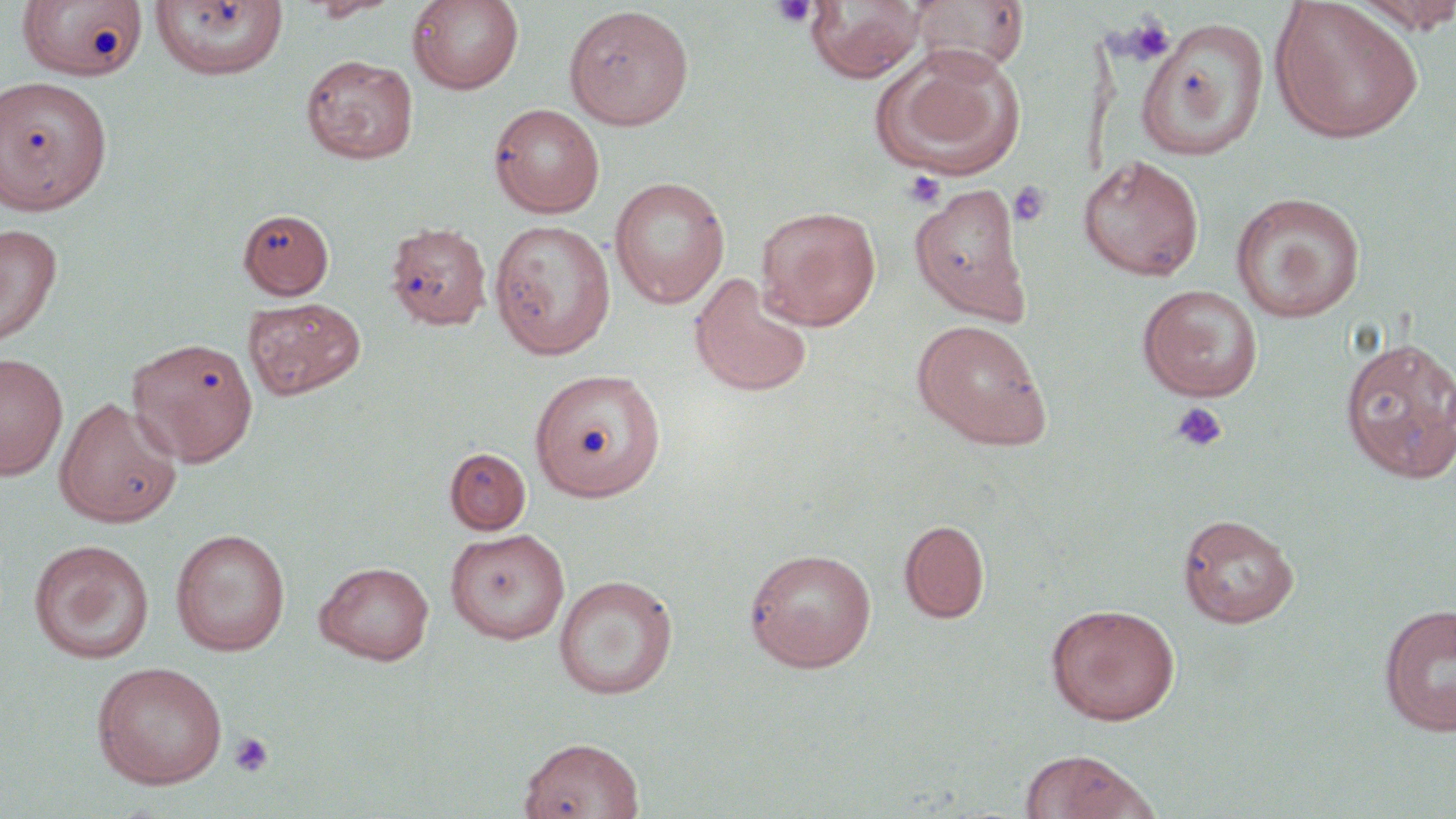

Summary:
  - Coordinate format: approximate bounding boxes as [x1, y1, x2, y2] in pixels
  - Platelet locations: [772, 0, 819, 27], [1119, 12, 1176, 65], [903, 171, 946, 208], [1008, 181, 1051, 227], [1171, 402, 1228, 453], [228, 732, 274, 777]
  - Uninfected red blood cell locations: [18, 0, 147, 82], [302, 0, 401, 22], [407, 0, 524, 94], [907, 0, 1030, 76], [149, 1, 289, 81], [806, 1, 924, 82], [1269, 1, 1424, 145], [1350, 1, 1456, 33], [563, 5, 694, 129], [1136, 17, 1270, 160], [872, 48, 1024, 180], [300, 53, 419, 164], [0, 76, 112, 216], [488, 103, 604, 218], [1078, 153, 1205, 282], [609, 176, 729, 309], [909, 183, 1031, 324], [1230, 192, 1366, 323], [755, 205, 881, 330], [238, 208, 335, 300], [489, 219, 616, 359], [384, 220, 493, 331], [0, 223, 62, 346], [689, 272, 814, 398], [1136, 283, 1264, 401], [243, 297, 366, 400], [911, 318, 1052, 450], [1338, 335, 1456, 483], [126, 337, 258, 467], [0, 352, 68, 480], [530, 368, 666, 501], [53, 397, 183, 527], [444, 447, 531, 534], [1178, 513, 1299, 628], [899, 519, 990, 623], [445, 527, 570, 644], [169, 528, 291, 656], [29, 539, 154, 664], [744, 547, 877, 672], [314, 560, 435, 665], [554, 574, 678, 699], [1378, 602, 1456, 737], [1046, 603, 1181, 725], [91, 660, 228, 789], [518, 736, 645, 819], [1020, 749, 1162, 819]
  - Slide-level diagnosis: no evidence of blood parasites
  - Stain: May-Grünwald-Giemsa
  - Modality: light microscopy
  - Magnification: 1000x
  - Field of view: single
  - Preparation: thin blood smear
  - Image size: 1456×819 pixels